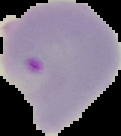
Malaria status: parasitized. Cell region segmented out of the field of view; the surrounding area is masked to black. Image is 121×136 pixels. From a thin blood smear.